Name the cell type shown.
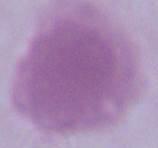

This is an erythrocyte.

{
  "magnification": "1000x",
  "modality": "micrograph"
}